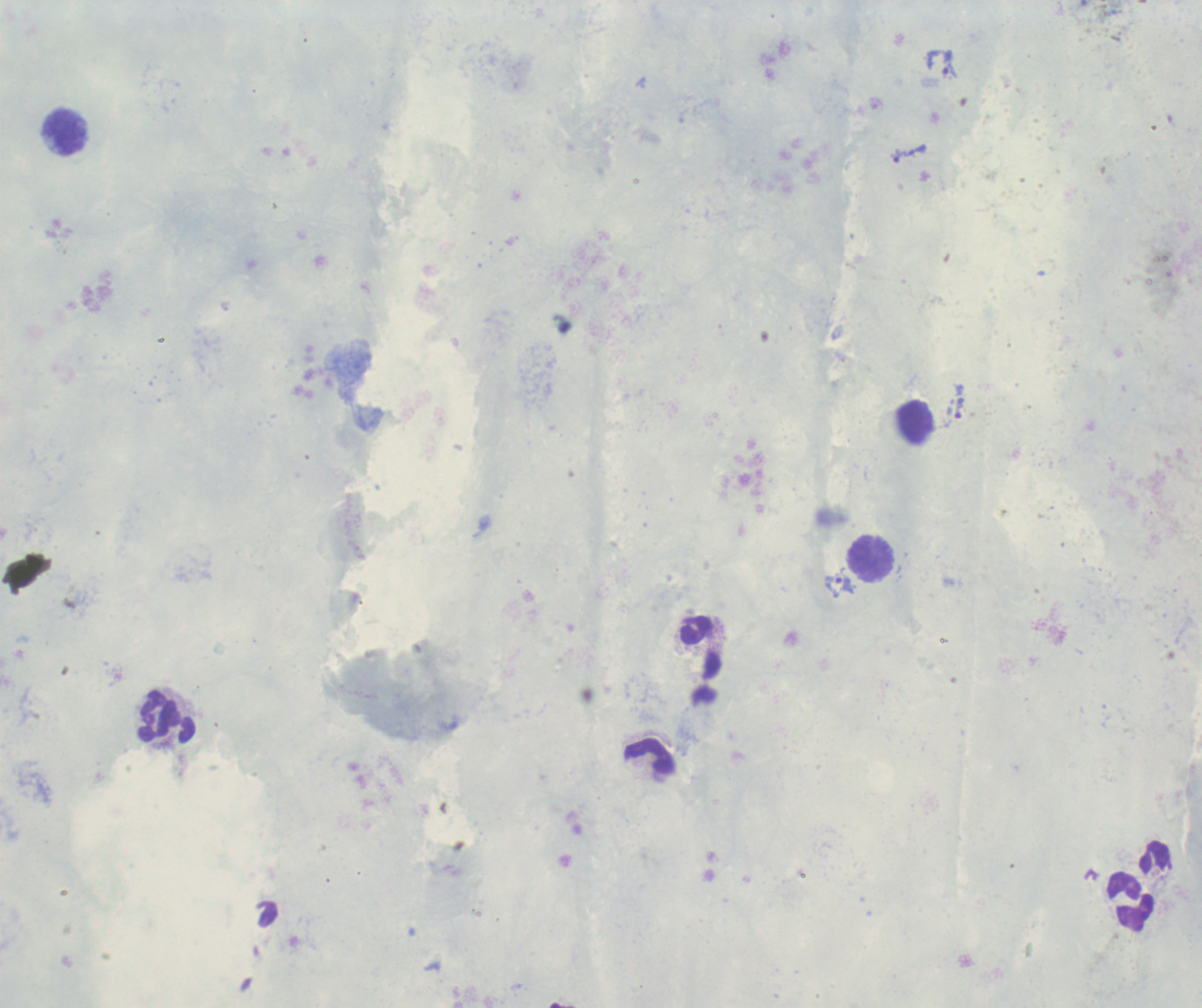
field_of_view: single
trophozoite_locations: 'approximate centers as [x, y] in pixels: [949, 64], [909, 153], [958, 410], [840, 582]'
leukocyte_locations: 'approximate centers as [x, y] in pixels: [65, 133], [914, 423], [870, 559], [166, 717], [649, 757], [1130, 901]'
coloration_quality: good
magnification: 100x
stain: Romanowsky
background_quality: poor
context: previously used in an actual diagnosis
image_size: 1202×1008 pixels
result: malaria parasites identified
preparation: thick blood smear